Locate and identify every blood parasite.
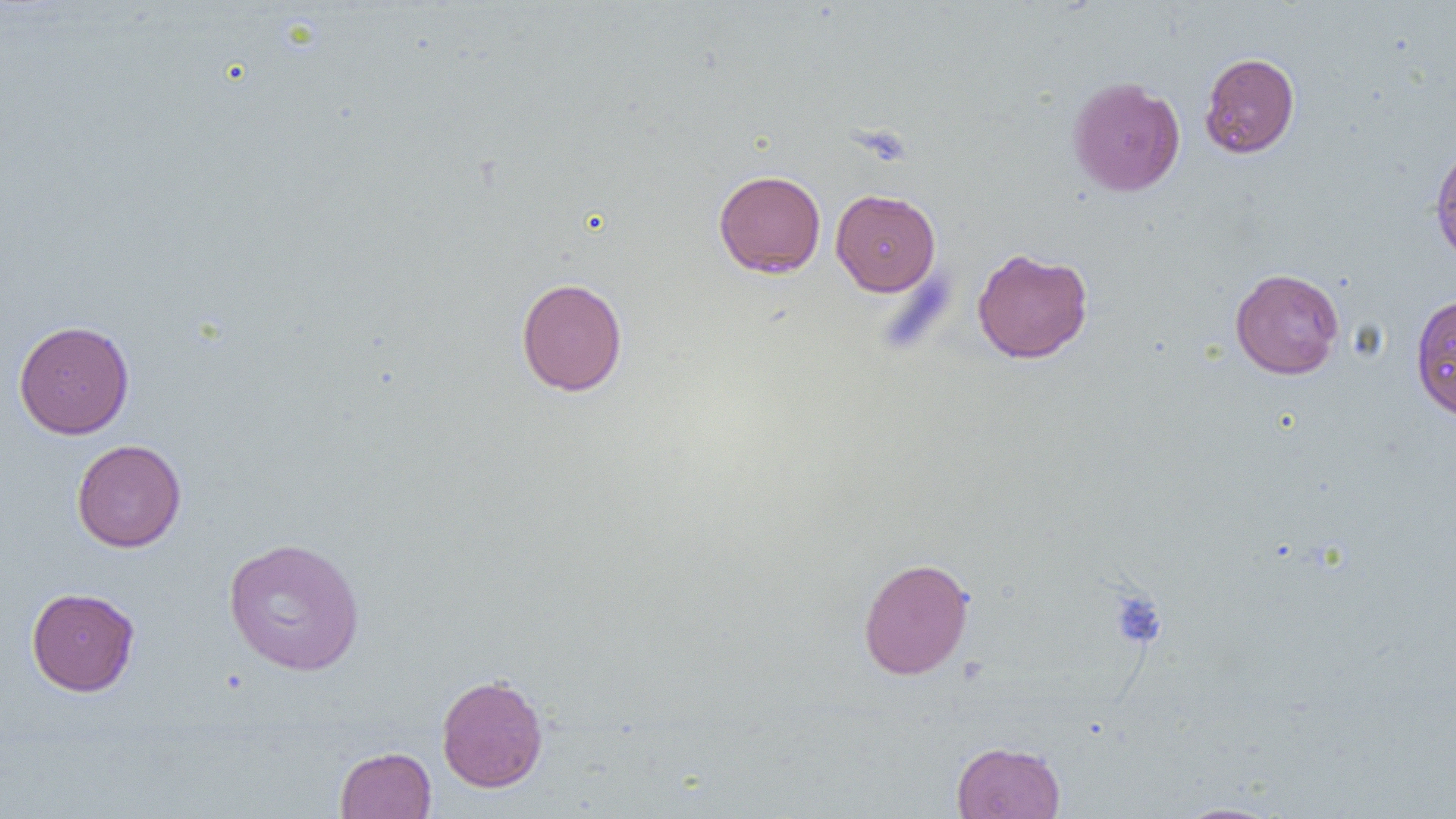

No blood parasites seen.

Summary:
  - Coordinate format: approximate bounding boxes as named x1/y1/x2/y2 corners in pixels
  - Uninfected red blood cell locations: (x1=1200, y1=52, x2=1300, y2=159), (x1=1067, y1=76, x2=1185, y2=197), (x1=1430, y1=142, x2=1456, y2=265), (x1=713, y1=169, x2=826, y2=278), (x1=830, y1=188, x2=940, y2=296), (x1=972, y1=247, x2=1093, y2=364), (x1=1230, y1=267, x2=1344, y2=379), (x1=516, y1=277, x2=628, y2=396), (x1=1410, y1=292, x2=1455, y2=421), (x1=14, y1=319, x2=134, y2=439), (x1=71, y1=438, x2=186, y2=552), (x1=223, y1=536, x2=365, y2=676), (x1=858, y1=557, x2=974, y2=680), (x1=26, y1=587, x2=140, y2=696), (x1=436, y1=673, x2=548, y2=792), (x1=951, y1=740, x2=1066, y2=819), (x1=335, y1=746, x2=436, y2=818), (x1=1171, y1=801, x2=1286, y2=819)
  - Platelet locations: (x1=1109, y1=589, x2=1167, y2=650)
  - Slide-level diagnosis: negative for blood parasites
  - Preparation: thin blood film
  - Image size: 1456×819 pixels
  - Magnification: 1000x
  - Field of view: one of a larger specimen
  - Modality: optical microscopy